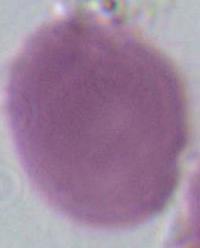

Summary:
  - Modality: micrograph
  - Identification: red blood cell
  - Magnification: 1000x